Assess the morphology of the erythrocytes.
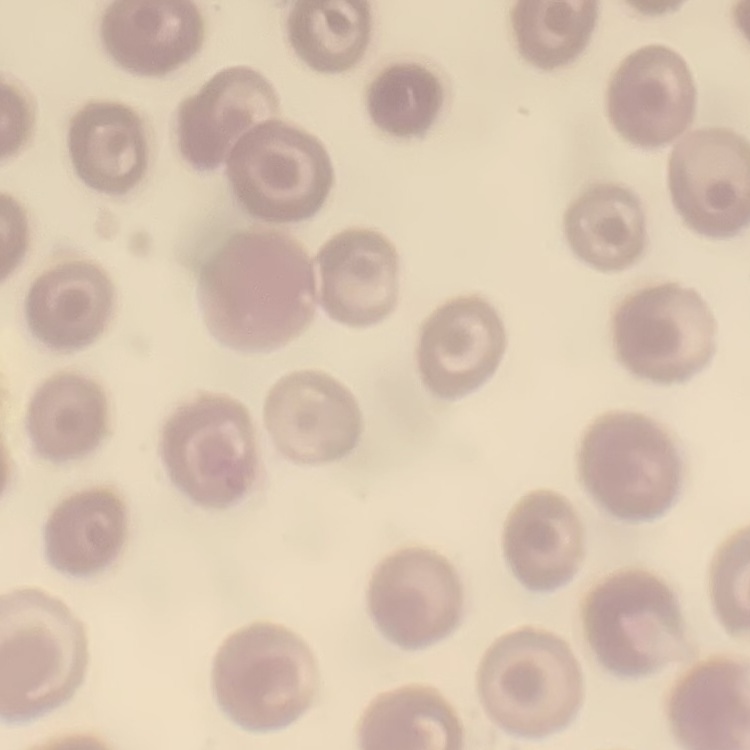
No rouleaux formation.

stain: Field's or Giemsa
preparation: thin peripheral smear
image_type: square crop of a larger photomicrograph